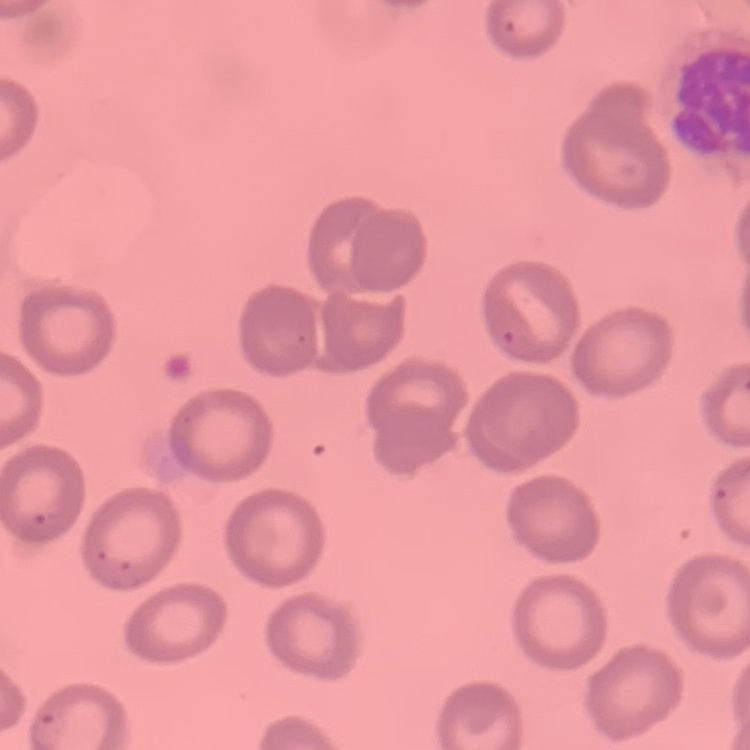 The red blood cells show no rouleaux formation. Square crop of a larger photomicrograph. Stained with either Field's or Giemsa. Thin blood film.